Locate every blood parasite and identify its species.
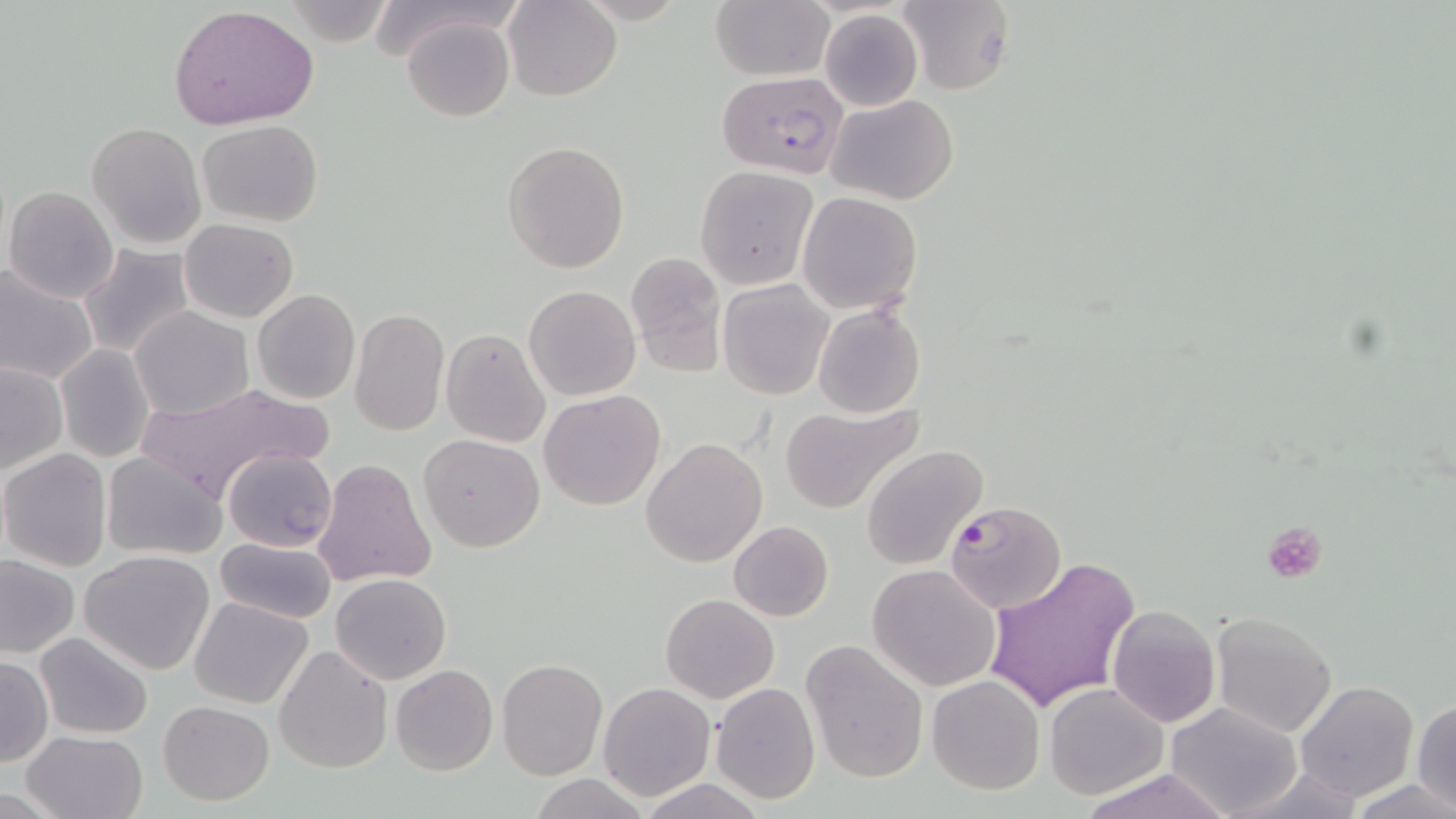
Approximate bounding boxes as (x1, y1, x2, y2) in pixels.
Plasmodium falciparum-infected red blood cells: (716, 72, 851, 182), (945, 500, 1068, 612).
No Plasmodium ovale, Plasmodium malariae, Plasmodium vivax, Babesia divergens, or Trypanosoma brucei observed.

Platelet locations: (1264, 522, 1328, 585). Uninfected red blood cell locations: (504, 0, 622, 100), (897, 0, 1016, 95), (710, 1, 833, 81), (284, 2, 400, 47), (170, 6, 319, 130), (819, 9, 923, 111), (402, 14, 515, 121), (828, 93, 958, 206), (198, 119, 325, 226), (87, 121, 206, 249), (502, 141, 630, 273), (694, 164, 818, 290), (4, 186, 119, 303), (798, 191, 923, 315), (179, 218, 298, 322), (78, 244, 196, 361), (625, 250, 728, 375), (0, 264, 99, 386), (718, 278, 833, 401), (523, 283, 641, 401), (252, 290, 360, 404), (812, 300, 925, 419), (130, 306, 254, 419), (349, 307, 450, 437), (442, 328, 551, 447), (55, 344, 156, 463), (0, 363, 68, 474), (136, 381, 331, 502), (539, 389, 666, 511), (778, 402, 924, 515), (418, 433, 545, 552), (641, 438, 768, 568), (861, 446, 986, 571), (223, 447, 338, 551), (0, 449, 113, 572), (101, 452, 227, 561), (314, 459, 435, 589), (728, 521, 834, 621), (213, 537, 337, 624), (80, 550, 216, 674), (2, 556, 79, 658), (985, 556, 1142, 716), (867, 563, 1002, 692), (332, 573, 452, 684), (661, 593, 780, 703), (190, 597, 312, 709), (1106, 606, 1222, 727), (1210, 610, 1339, 738), (35, 632, 154, 739), (799, 638, 930, 784), (273, 643, 393, 773), (0, 657, 51, 766), (497, 657, 607, 780), (390, 664, 497, 775), (926, 674, 1045, 796), (597, 681, 717, 801), (1295, 681, 1419, 803), (711, 682, 821, 804), (1044, 682, 1168, 801), (1411, 699, 1456, 812), (157, 700, 275, 804), (1164, 701, 1304, 819), (22, 730, 147, 819), (1231, 764, 1366, 818), (1076, 769, 1233, 819), (531, 774, 651, 818), (639, 778, 767, 818), (1351, 778, 1455, 817). Slide-level diagnosis: Plasmodium falciparum. 1000x magnification. Thin blood film. Optical microscopy. Single field of view. Image is 1456×819 pixels. May-Grünwald-Giemsa stain.